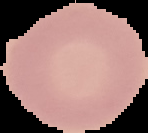
preparation = thin blood film
image type = cell region segmented out of the field of view; surrounding area masked to black
malaria status = uninfected
image size = 148×133 pixels